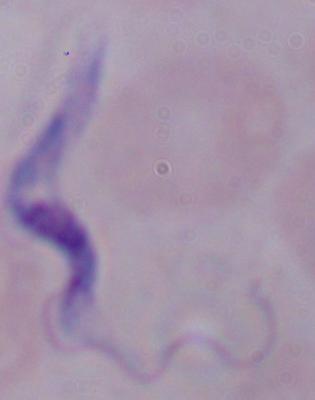
Captured at 1000x magnification. Photomicrograph. A trypanosome is seen.